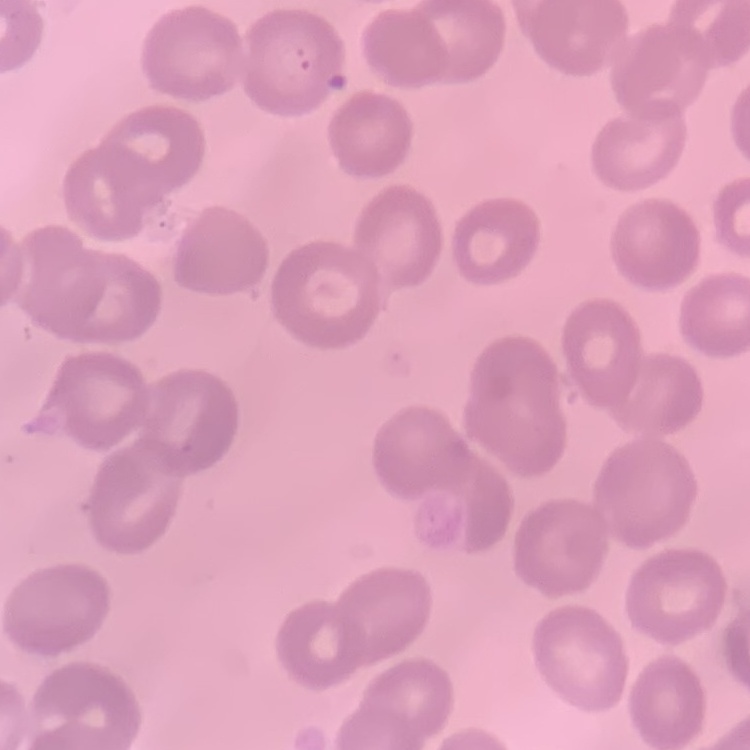
erythrocyte morphology = no rouleaux formation
preparation = thin peripheral smear
image type = one tile cut from a larger photomicrograph
stain = Field's or Giemsa